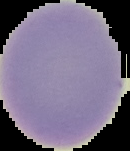 Result: negative for malaria parasites. Image is 130×151 pixels. Cell region segmented out of the field of view; the surrounding area is masked to black. From a thin blood film.